Assess the morphology of the red blood cells.
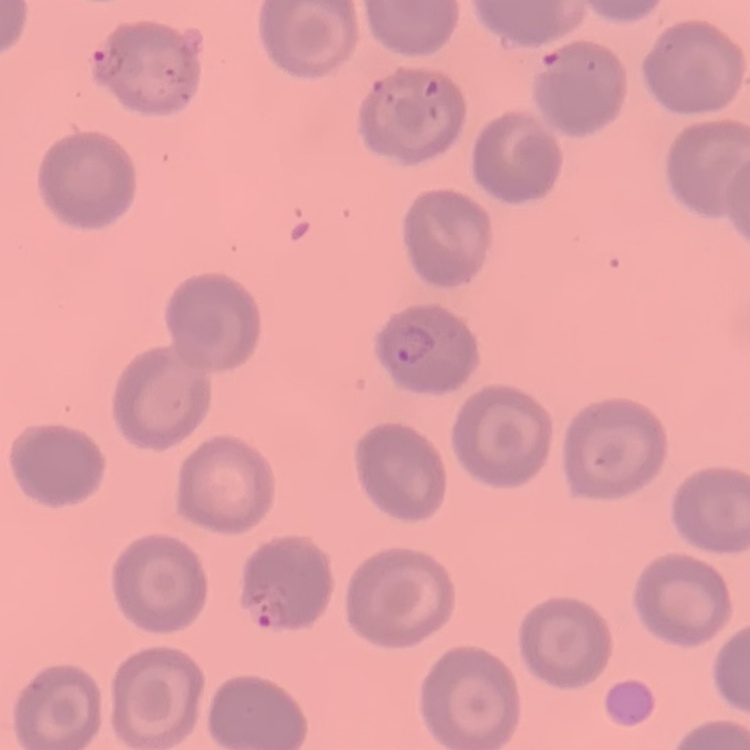
They show no rouleaux formation.

Summary:
  - Preparation: thin blood smear
  - Image type: one tile cut from a larger photomicrograph
  - Stain: Field's or Giemsa